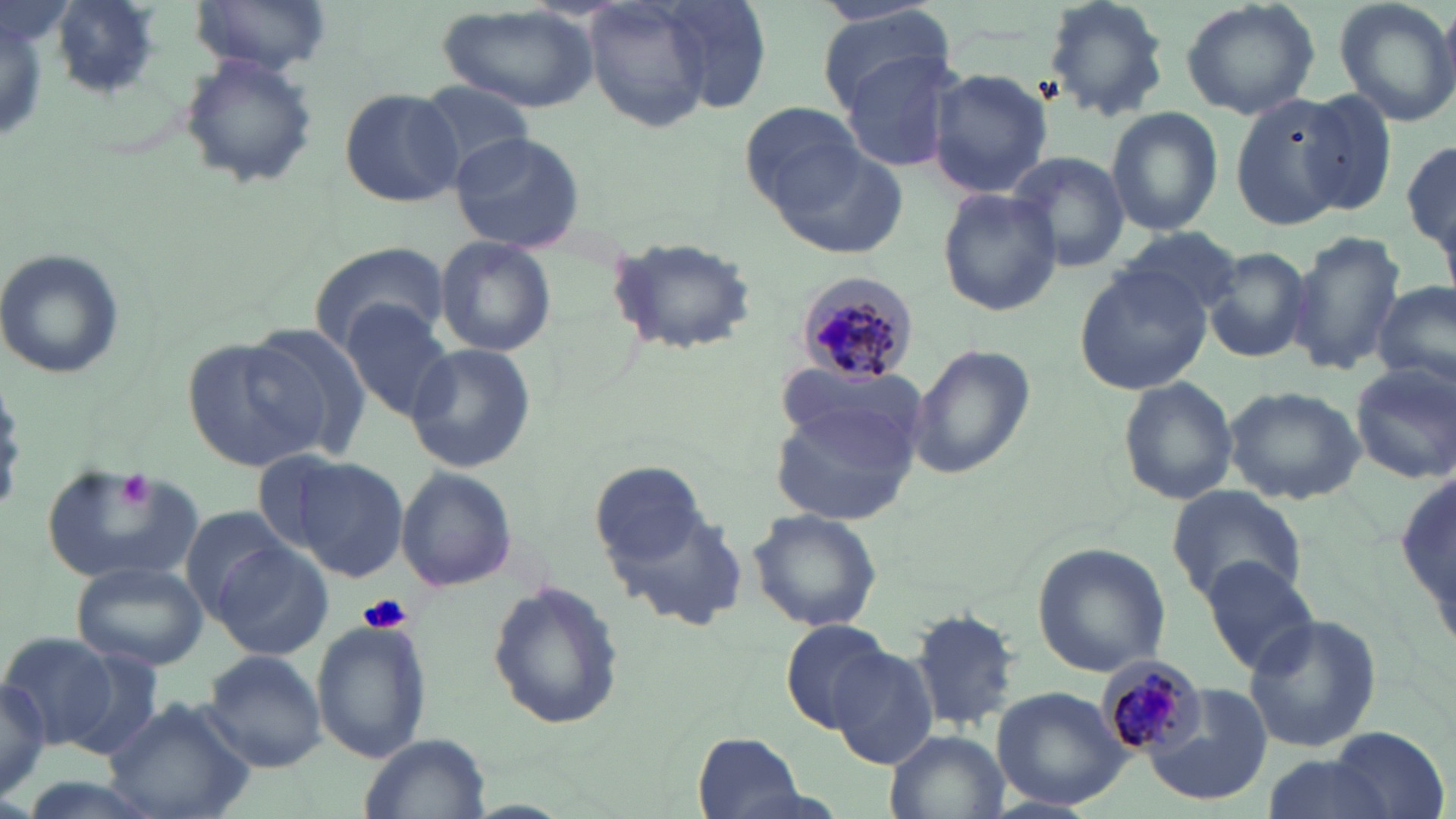
Summary:
  - Coordinate format: approximate bounding boxes as [x1, y1, x2, y2] in pixels
  - Uninfected red blood cell locations: [189, 0, 332, 77], [582, 0, 718, 134], [1042, 0, 1171, 119], [1178, 0, 1320, 121], [1332, 0, 1456, 129], [47, 1, 161, 101], [655, 2, 771, 113], [435, 3, 600, 114], [813, 9, 954, 108], [836, 43, 968, 177], [179, 50, 318, 190], [926, 67, 1055, 200], [411, 81, 542, 178], [339, 86, 465, 208], [1297, 90, 1400, 217], [1230, 95, 1350, 228], [741, 103, 868, 209], [1104, 106, 1223, 236], [449, 131, 586, 253], [1403, 131, 1455, 276], [767, 136, 911, 261], [1008, 150, 1130, 273], [936, 187, 1063, 318], [1115, 226, 1245, 318], [1285, 228, 1406, 377], [606, 236, 762, 357], [435, 239, 556, 355], [310, 245, 444, 349], [0, 248, 126, 380], [1205, 248, 1313, 364], [1074, 263, 1211, 394], [1374, 280, 1456, 395], [341, 302, 458, 422], [242, 322, 374, 460], [183, 336, 329, 472], [405, 344, 534, 473], [910, 345, 1034, 480], [1350, 363, 1455, 485], [774, 364, 924, 464], [1116, 376, 1240, 505], [1223, 387, 1365, 503], [770, 405, 920, 526], [289, 457, 409, 582], [39, 459, 204, 584], [1397, 461, 1454, 654], [591, 462, 708, 567], [396, 467, 517, 593], [1167, 484, 1307, 605], [600, 486, 750, 632], [178, 506, 300, 623], [748, 509, 883, 634], [207, 540, 333, 658], [1034, 543, 1171, 677], [1205, 557, 1325, 676], [72, 558, 210, 671], [486, 581, 624, 731], [910, 606, 1022, 731], [1242, 613, 1383, 754], [311, 616, 431, 766], [780, 618, 895, 733], [1, 630, 122, 754], [829, 646, 937, 770], [200, 647, 328, 773], [0, 674, 52, 803], [1143, 683, 1274, 804], [993, 685, 1134, 810], [103, 696, 256, 818], [1328, 726, 1449, 819], [884, 729, 1008, 819], [361, 733, 491, 819], [694, 733, 804, 817], [1258, 753, 1396, 819]
  - Platelet locations: [119, 469, 153, 510], [357, 593, 413, 635]
  - Plasmodium malariae-infected red blood cell locations: [796, 273, 920, 386], [1096, 655, 1204, 756]
  - Slide-level diagnosis: Plasmodium malariae
  - Preparation: thin blood smear
  - Field of view: one of a larger specimen
  - Modality: optical microscopy
  - Stain: May-Grünwald-Giemsa
  - Magnification: 1000x
  - Image size: 1456×819 pixels